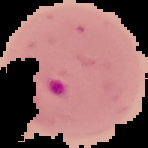

preparation: thin blood film
image_type: segmented cell region with the area outside set to black
image_size: 148×148 pixels
malaria_status: parasitized